Name the cell type shown.
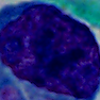
A leukocyte.

{
  "magnification": "1000x",
  "modality": "photomicrograph"
}